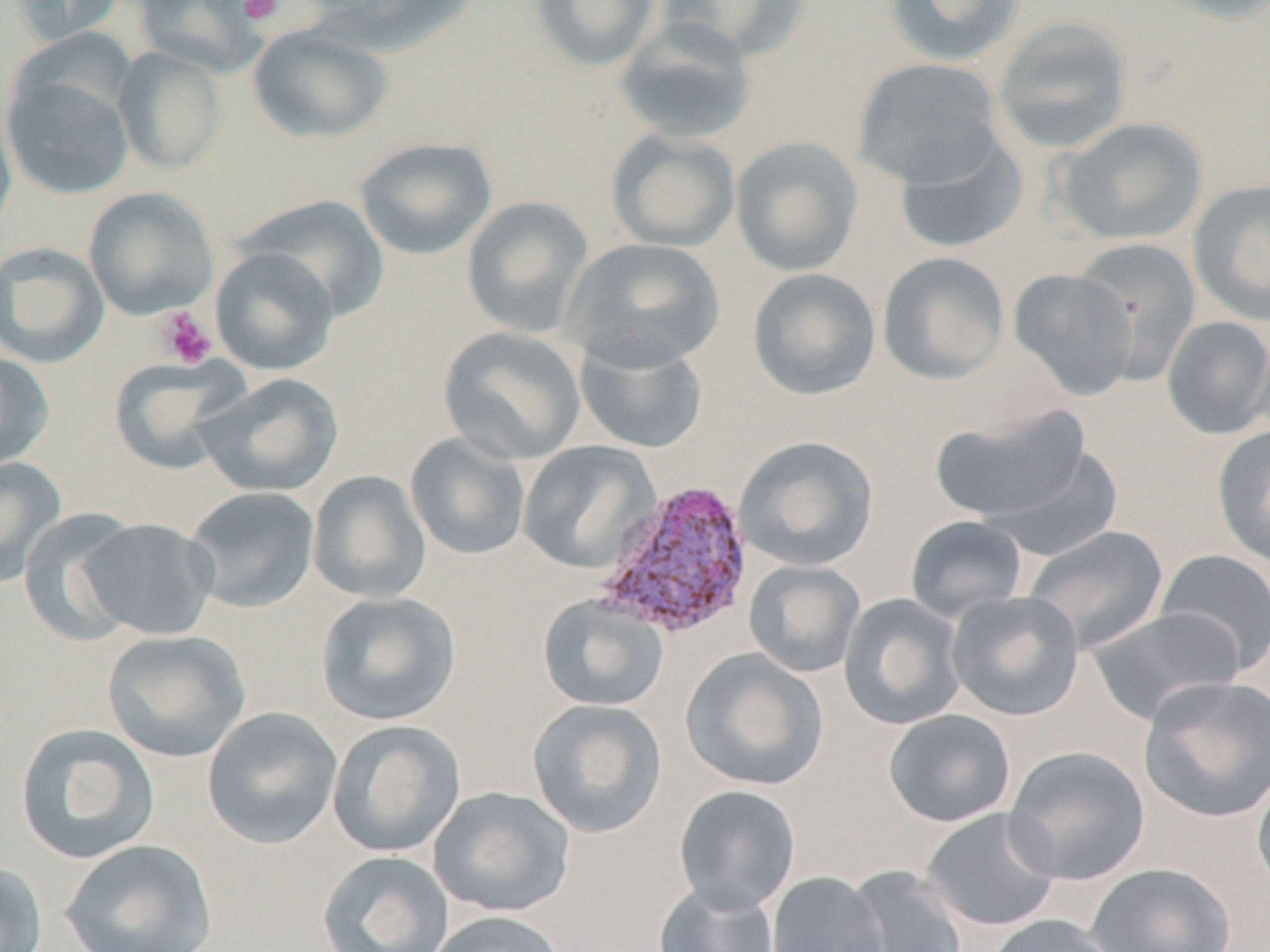
slide_level_diagnosis: Plasmodium vivax
stain: May-Grünwald-Giemsa
modality: optical microscopy
plasmodium_vivax_infected_red_blood_cell_locations: 'approximate bounding boxes as named x1/y1/x2/y2 corners in pixels: (x1=594, y1=479, x2=756, y2=642)'
magnification: 1000x
uninfected_red_blood_cell_locations: 'approximate bounding boxes as named x1/y1/x2/y2 corners in pixels: (x1=7, y1=0, x2=126, y2=45), (x1=133, y1=0, x2=267, y2=76), (x1=298, y1=0, x2=487, y2=56), (x1=528, y1=0, x2=662, y2=71), (x1=659, y1=0, x2=812, y2=63), (x1=883, y1=0, x2=1026, y2=67), (x1=1150, y1=0, x2=1270, y2=26), (x1=992, y1=16, x2=1133, y2=154), (x1=614, y1=18, x2=759, y2=144), (x1=247, y1=23, x2=394, y2=143), (x1=114, y1=47, x2=226, y2=174), (x1=852, y1=57, x2=1005, y2=189), (x1=1, y1=69, x2=135, y2=200), (x1=0, y1=94, x2=18, y2=244), (x1=1054, y1=116, x2=1208, y2=246), (x1=606, y1=129, x2=741, y2=253), (x1=892, y1=131, x2=1028, y2=254), (x1=730, y1=136, x2=864, y2=277), (x1=354, y1=137, x2=497, y2=260), (x1=1188, y1=178, x2=1270, y2=327), (x1=83, y1=186, x2=219, y2=320), (x1=241, y1=195, x2=390, y2=322), (x1=461, y1=196, x2=593, y2=339), (x1=563, y1=237, x2=726, y2=371), (x1=1072, y1=238, x2=1202, y2=385), (x1=0, y1=241, x2=109, y2=368), (x1=209, y1=247, x2=339, y2=376), (x1=877, y1=251, x2=1010, y2=384), (x1=747, y1=267, x2=881, y2=401), (x1=1008, y1=267, x2=1140, y2=401), (x1=1162, y1=315, x2=1270, y2=440), (x1=1251, y1=323, x2=1270, y2=448), (x1=438, y1=326, x2=587, y2=464), (x1=574, y1=333, x2=709, y2=455), (x1=0, y1=351, x2=54, y2=470), (x1=108, y1=356, x2=248, y2=475), (x1=197, y1=372, x2=344, y2=497), (x1=930, y1=405, x2=1092, y2=526), (x1=1212, y1=424, x2=1270, y2=568), (x1=405, y1=432, x2=531, y2=561), (x1=734, y1=435, x2=879, y2=572), (x1=517, y1=441, x2=661, y2=574), (x1=988, y1=441, x2=1125, y2=559), (x1=0, y1=456, x2=67, y2=586), (x1=307, y1=470, x2=432, y2=603), (x1=183, y1=486, x2=319, y2=613), (x1=19, y1=508, x2=145, y2=647), (x1=904, y1=514, x2=1028, y2=622), (x1=78, y1=518, x2=220, y2=640), (x1=1024, y1=525, x2=1169, y2=653), (x1=1154, y1=548, x2=1270, y2=674), (x1=744, y1=559, x2=866, y2=678), (x1=946, y1=590, x2=1085, y2=721), (x1=315, y1=591, x2=462, y2=726), (x1=839, y1=593, x2=968, y2=730), (x1=537, y1=594, x2=670, y2=712), (x1=1087, y1=606, x2=1244, y2=725), (x1=102, y1=629, x2=252, y2=762), (x1=681, y1=648, x2=830, y2=792), (x1=1138, y1=676, x2=1270, y2=823), (x1=527, y1=698, x2=668, y2=839), (x1=201, y1=706, x2=344, y2=850), (x1=883, y1=709, x2=1016, y2=827), (x1=327, y1=720, x2=467, y2=858), (x1=15, y1=723, x2=160, y2=863), (x1=1003, y1=745, x2=1150, y2=885), (x1=1252, y1=768, x2=1270, y2=894), (x1=673, y1=785, x2=802, y2=913), (x1=429, y1=786, x2=576, y2=917), (x1=920, y1=808, x2=1061, y2=932), (x1=59, y1=838, x2=218, y2=952), (x1=318, y1=849, x2=454, y2=952), (x1=0, y1=862, x2=48, y2=952), (x1=1086, y1=862, x2=1235, y2=952), (x1=841, y1=864, x2=968, y2=952), (x1=766, y1=871, x2=888, y2=952), (x1=653, y1=880, x2=782, y2=952), (x1=426, y1=910, x2=569, y2=952), (x1=982, y1=914, x2=1120, y2=952)'
field_of_view: single
image_size: 1270×952 pixels
preparation: thin blood film
platelet_locations: 'approximate bounding boxes as named x1/y1/x2/y2 corners in pixels: (x1=238, y1=0, x2=283, y2=25), (x1=155, y1=307, x2=217, y2=369)'